Assess this cell for malaria.
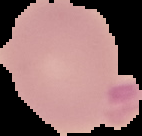

Uninfected.

From a thin blood film. Image is 142×136 pixels. The area outside the segmented cell region is set to black.